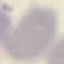 Result: no malaria parasites detected. Acquired by smartphone through the microscope eyepiece. Thin blood smear. Cell patch, automatically extracted from a larger field of view and resized to 64 × 64 pixels. Giemsa-stained preparation.